Comment on the morphology of the erythrocytes.
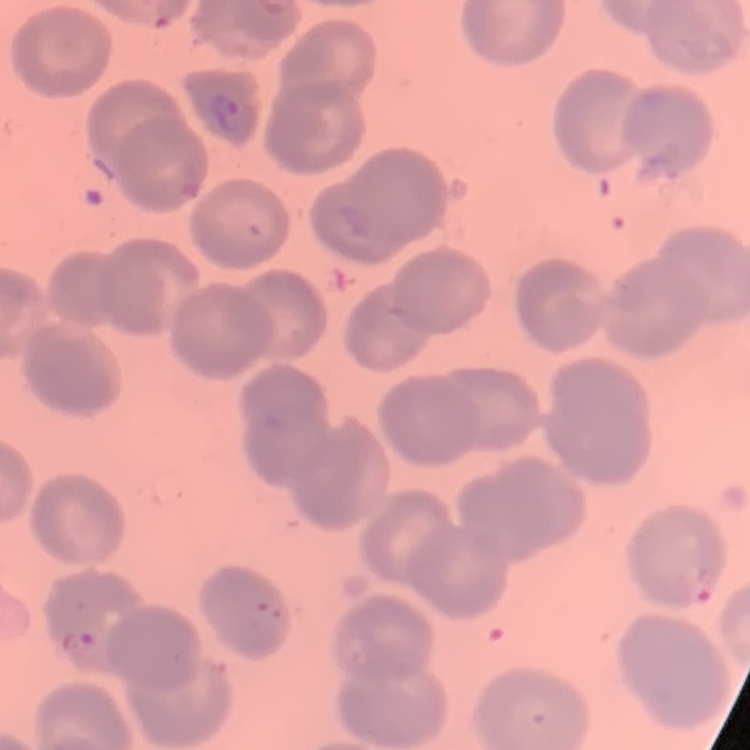
They show no rouleaux formation.

Thin blood smear. One tile cut from a larger photomicrograph. Stained with either Field's or Giemsa.